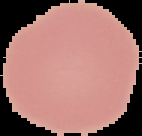

Summary:
  - Result: negative for Plasmodium parasites
  - Image size: 142×136 pixels
  - Image type: cell region segmented out of the field of view; surrounding area masked to black
  - Preparation: thin blood film